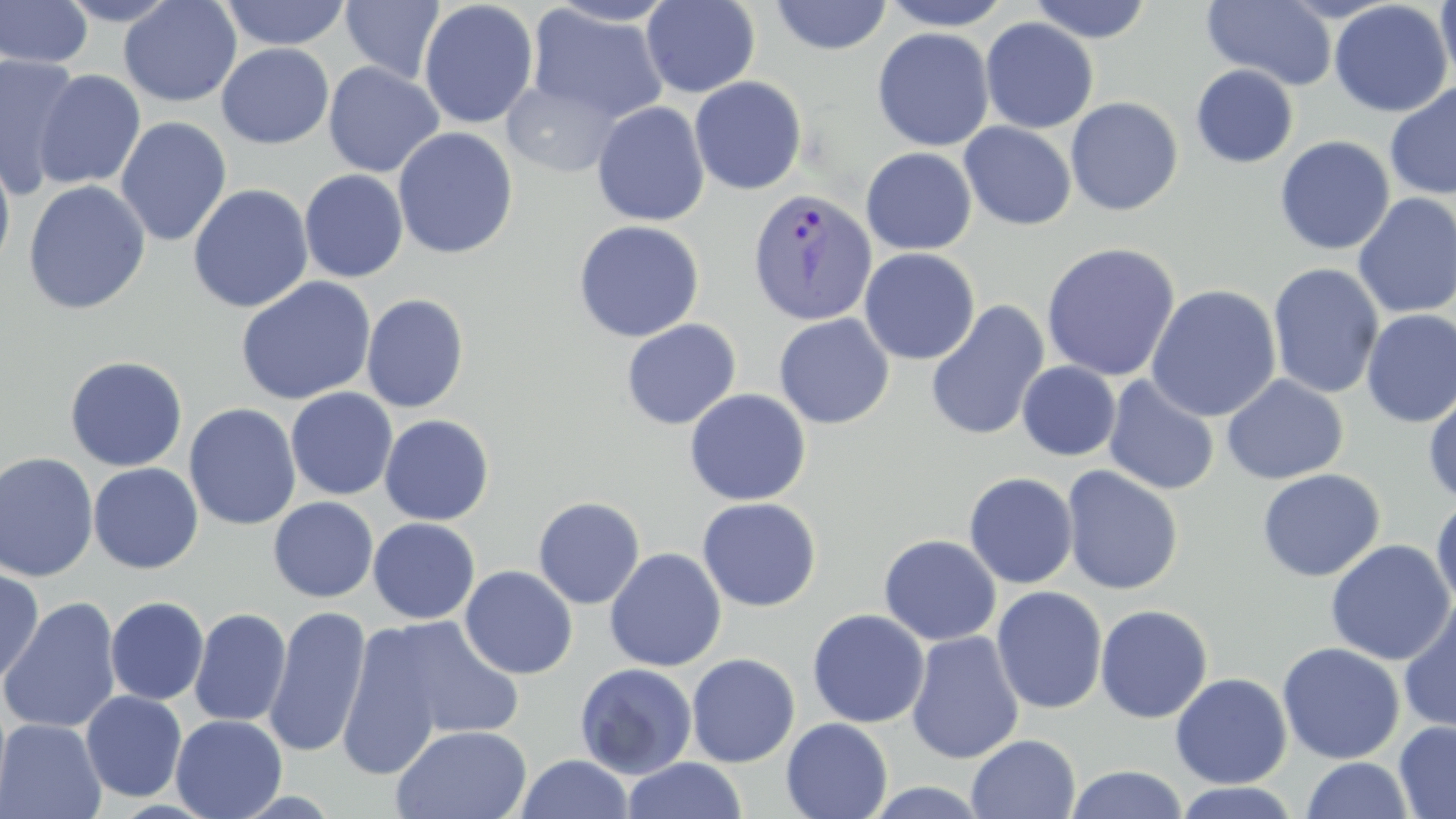

Summary:
  - Coordinate format: approximate bounding boxes as [x1, y1, x2, y2] in pixels
  - Plasmodium vivax-infected red blood cell locations: [747, 187, 877, 327]
  - Uninfected red blood cell locations: [0, 0, 94, 68], [55, 0, 183, 26], [118, 0, 242, 107], [218, 0, 351, 51], [340, 0, 445, 85], [418, 0, 539, 130], [641, 0, 760, 98], [769, 0, 892, 56], [877, 0, 1015, 31], [1027, 0, 1153, 43], [1202, 0, 1338, 90], [1436, 0, 1456, 87], [541, 1, 680, 28], [1329, 1, 1452, 117], [527, 4, 668, 126], [980, 17, 1099, 134], [872, 27, 994, 152], [216, 43, 334, 149], [0, 54, 82, 198], [323, 62, 444, 178], [1190, 64, 1299, 168], [33, 69, 146, 190], [689, 76, 807, 195], [501, 77, 624, 178], [1384, 82, 1456, 200], [1065, 97, 1183, 216], [592, 102, 710, 226], [115, 116, 232, 247], [959, 122, 1077, 230], [392, 126, 519, 260], [1274, 136, 1395, 255], [860, 147, 977, 255], [0, 151, 16, 277], [299, 156, 522, 276], [299, 169, 408, 283], [23, 180, 151, 316], [188, 183, 313, 313], [1352, 193, 1456, 319], [573, 220, 705, 342], [1041, 242, 1181, 382], [859, 247, 980, 365], [1268, 263, 1384, 400], [236, 276, 376, 406], [1145, 284, 1282, 422], [361, 293, 469, 413], [925, 300, 1050, 442], [1360, 309, 1456, 428], [774, 313, 894, 430], [621, 318, 741, 430], [64, 355, 188, 472], [1016, 361, 1121, 461], [1221, 374, 1349, 485], [1103, 375, 1220, 496], [1423, 384, 1456, 507], [285, 387, 398, 501], [685, 388, 811, 506], [184, 402, 301, 531], [379, 414, 494, 525], [0, 452, 99, 581], [87, 463, 204, 574], [1061, 465, 1184, 596], [1257, 468, 1386, 582], [980, 469, 1092, 712], [963, 472, 1078, 589], [1430, 494, 1456, 609], [532, 496, 645, 610], [268, 497, 379, 602], [697, 497, 822, 612], [368, 517, 480, 624], [879, 534, 1001, 646], [1325, 539, 1455, 665], [605, 548, 727, 672], [0, 565, 44, 686], [459, 565, 578, 679], [991, 586, 1108, 714], [105, 596, 209, 705], [0, 597, 122, 736], [1398, 598, 1456, 734], [1094, 604, 1213, 724], [263, 605, 372, 758], [189, 607, 291, 728], [807, 608, 930, 728], [374, 615, 527, 743], [335, 625, 446, 780], [906, 631, 1025, 765], [1277, 642, 1405, 764], [686, 653, 800, 767], [574, 662, 698, 779], [1170, 662, 1405, 775], [1170, 672, 1292, 789], [80, 690, 187, 802], [171, 714, 287, 818], [0, 718, 106, 819], [781, 718, 893, 819], [1394, 719, 1456, 819], [393, 724, 532, 819], [966, 733, 1081, 819], [514, 753, 634, 819], [621, 757, 747, 818], [1301, 757, 1413, 817], [1066, 765, 1188, 818], [862, 781, 994, 818], [1172, 782, 1302, 818]
  - Slide-level diagnosis: Plasmodium vivax
  - Preparation: thin blood film
  - Image size: 1456×819 pixels
  - Modality: optical microscopy
  - Field of view: one of a larger specimen
  - Stain: May-Grünwald-Giemsa
  - Magnification: 1000x